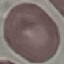 Malaria status: uninfected. Thin smear of blood. Photographed with a smartphone camera at the microscope eyepiece. Cell patch, automatically extracted from a larger field of view and resized to 64 × 64 pixels. Giemsa-stained preparation.